State which parasite is depicted.
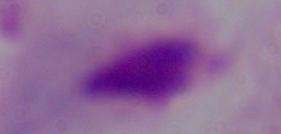
This is a trichomonad.

modality = photomicrograph
magnification = 1000x